Name the parasite shown.
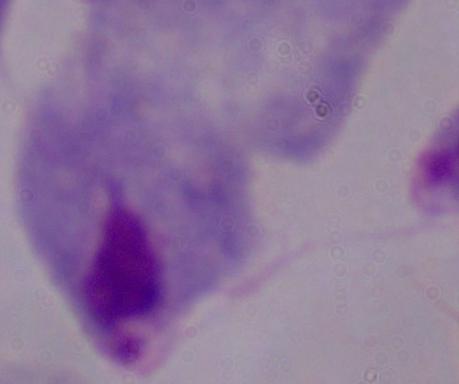
A trichomonad.

Summary:
  - Magnification: 1000x
  - Modality: photomicrograph